Identify the parasite.
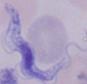
This is a trypanosome.

1000x magnification. Micrograph.